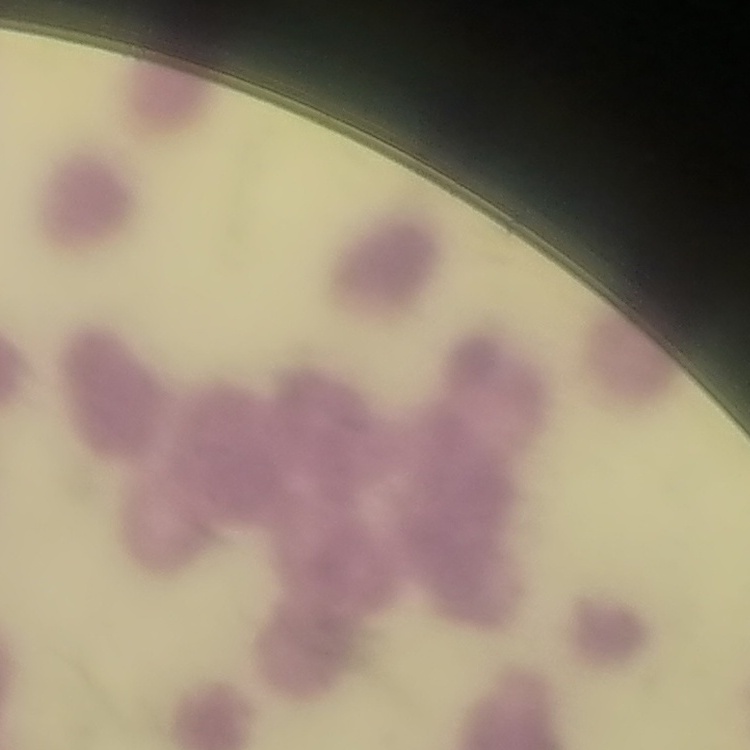

The red blood cells show rouleaux formation. Thin blood film. One tile cut from a larger photomicrograph. Stained with either Field's or Giemsa.